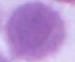

identification: red blood cell
magnification: 1000x
modality: micrograph